Identify the parasite.
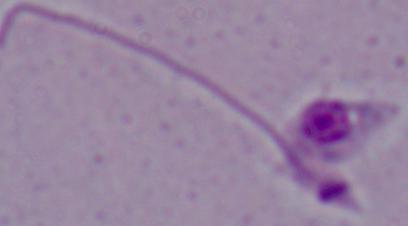
This is Leishmania.

Summary:
  - Magnification: 1000x
  - Modality: photomicrograph